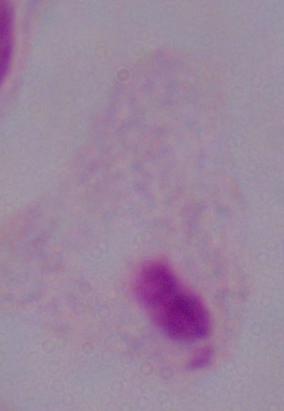

{
  "identification": "trichomonad",
  "modality": "photomicrograph",
  "magnification": "1000x"
}